Name the cell type shown.
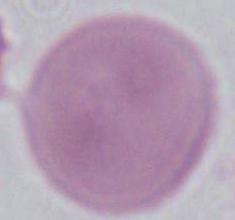

This is an erythrocyte.

modality = micrograph
magnification = 1000x